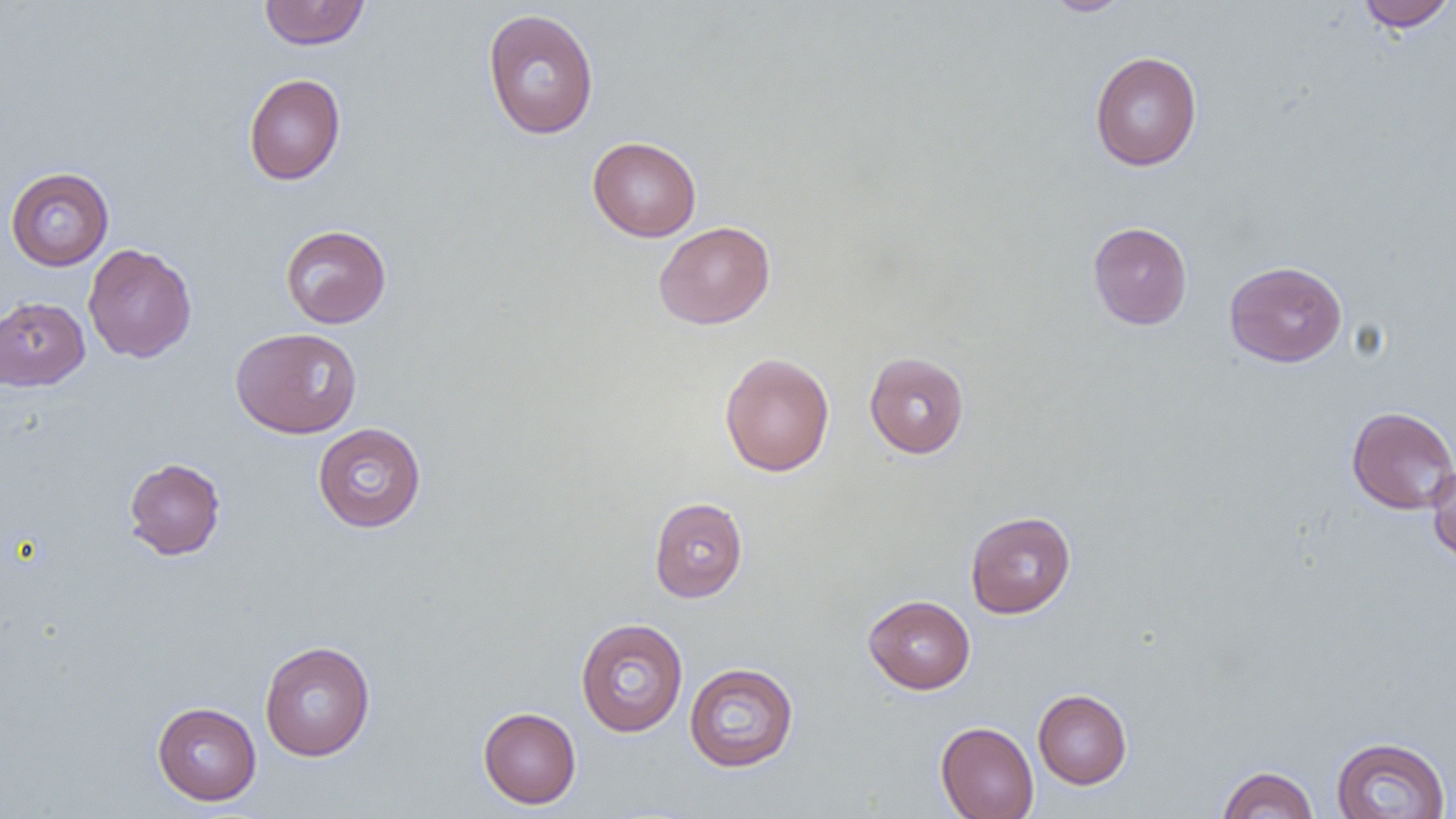

slide_level_diagnosis: no evidence of blood parasites
modality: light microscopy
field_of_view: one of a larger specimen
image_size: 1456×819 pixels
preparation: thin blood film
uninfected_red_blood_cell_locations: 'approximate bounding boxes as (x1, y1, x2, y2) in pixels: (258, 0, 370, 50), (1044, 0, 1132, 16), (1355, 0, 1455, 32), (482, 8, 599, 139), (1089, 51, 1202, 171), (244, 73, 346, 185), (587, 136, 702, 242), (5, 166, 114, 270), (653, 221, 776, 329), (1088, 222, 1193, 329), (280, 224, 391, 328), (82, 243, 197, 363), (1224, 260, 1347, 367), (0, 297, 90, 391), (231, 327, 362, 438), (719, 352, 835, 476), (864, 352, 970, 458), (1346, 406, 1456, 514), (312, 422, 426, 533), (124, 457, 225, 560), (1426, 463, 1456, 563), (648, 496, 748, 602), (965, 511, 1076, 618), (863, 594, 975, 694), (575, 618, 688, 736), (259, 640, 376, 761), (684, 662, 799, 772), (1033, 689, 1132, 789), (152, 701, 261, 805), (478, 706, 581, 808), (935, 721, 1039, 819), (1331, 736, 1450, 819), (1217, 766, 1318, 819)'
magnification: 1000x